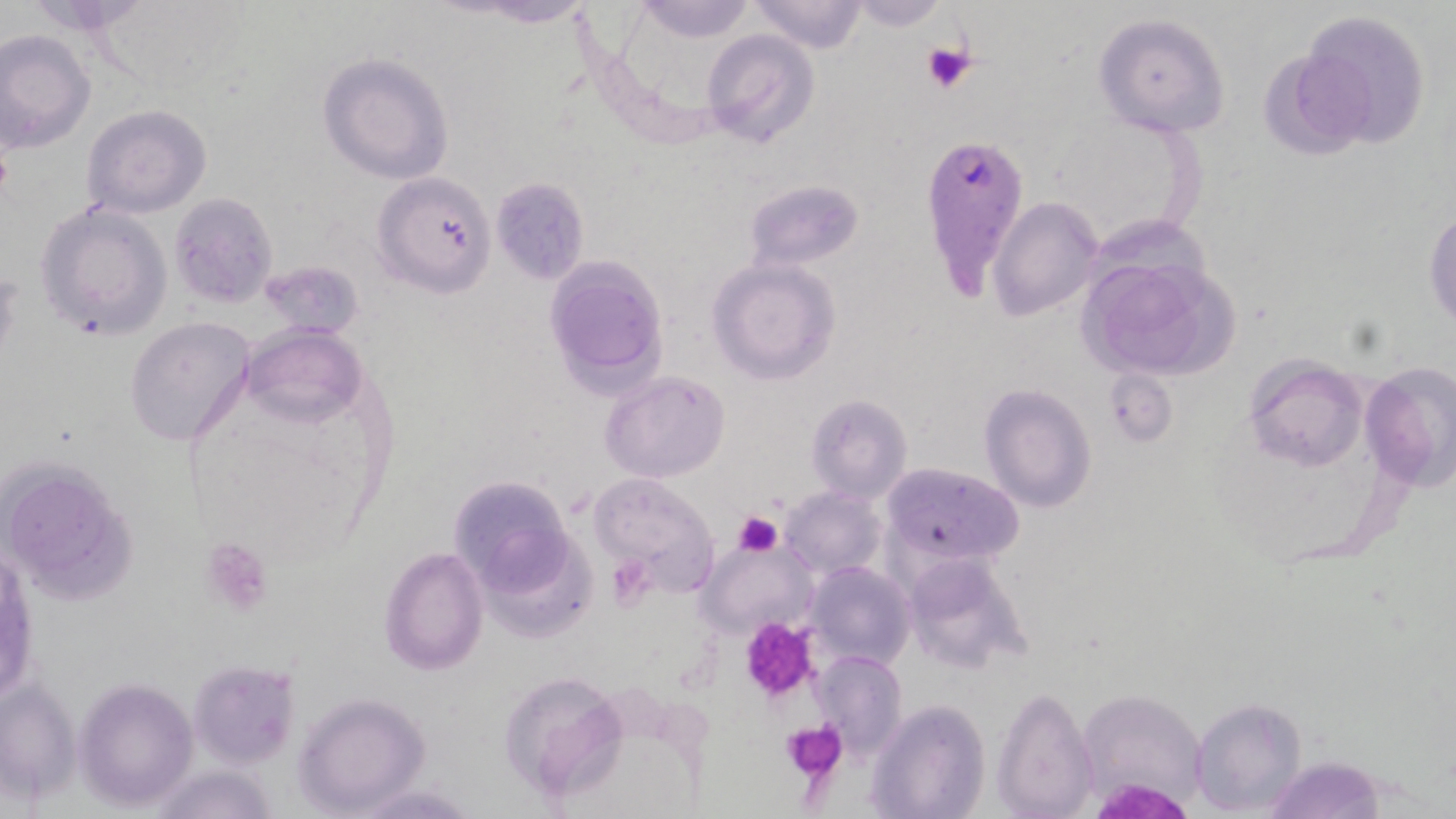

Approximate bounding boxes as (x1, y1, x2, y2) in pixels. Uninfected red blood cell locations: (16, 0, 157, 38), (450, 0, 602, 30), (630, 0, 758, 42), (750, 0, 871, 53), (842, 0, 949, 30), (1296, 10, 1433, 149), (1093, 12, 1232, 138), (0, 29, 96, 154), (700, 30, 820, 149), (317, 52, 454, 184), (82, 104, 212, 219), (371, 171, 496, 296), (491, 179, 590, 283), (747, 179, 864, 269), (169, 192, 278, 309), (989, 199, 1102, 320), (34, 202, 172, 340), (1425, 208, 1456, 330), (1075, 246, 1233, 382), (544, 255, 671, 389), (707, 258, 842, 386), (254, 259, 365, 339), (125, 316, 255, 448), (242, 323, 367, 427), (1244, 354, 1367, 474), (1359, 360, 1455, 490), (1104, 368, 1178, 447), (601, 370, 730, 482), (980, 383, 1097, 513), (806, 394, 912, 503), (0, 456, 140, 607), (882, 462, 1024, 569), (589, 473, 720, 591), (448, 474, 578, 595), (781, 487, 886, 580), (474, 524, 596, 646), (698, 537, 818, 640), (378, 545, 487, 676), (901, 552, 1033, 674), (806, 560, 915, 671), (814, 651, 906, 757), (187, 660, 299, 768), (497, 671, 628, 802), (0, 676, 81, 805), (74, 678, 198, 812), (993, 684, 1097, 819), (1078, 686, 1208, 811), (292, 692, 432, 815), (1191, 697, 1307, 817), (867, 699, 989, 819), (1266, 755, 1387, 818), (145, 763, 279, 819), (349, 782, 481, 816). Plasmodium falciparum-infected red blood cell locations: (917, 132, 1026, 296). Platelet locations: (921, 43, 977, 95), (733, 511, 783, 557), (199, 537, 274, 617), (607, 554, 656, 609), (740, 619, 819, 703), (782, 719, 846, 779). Slide-level diagnosis: Plasmodium falciparum. May-Grünwald-Giemsa-stained preparation. Captured at 1000x magnification. Thin blood film. Image is 1456×819 pixels. Optical microscopy. Single field of view.